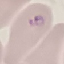 Malaria status: parasitized. Automatically extracted cell patch, resized to 64 × 64 pixels. Thin smear of blood. Photographed with a smartphone camera at the microscope eyepiece. Giemsa stain.